Outline each blood parasite and name the species.
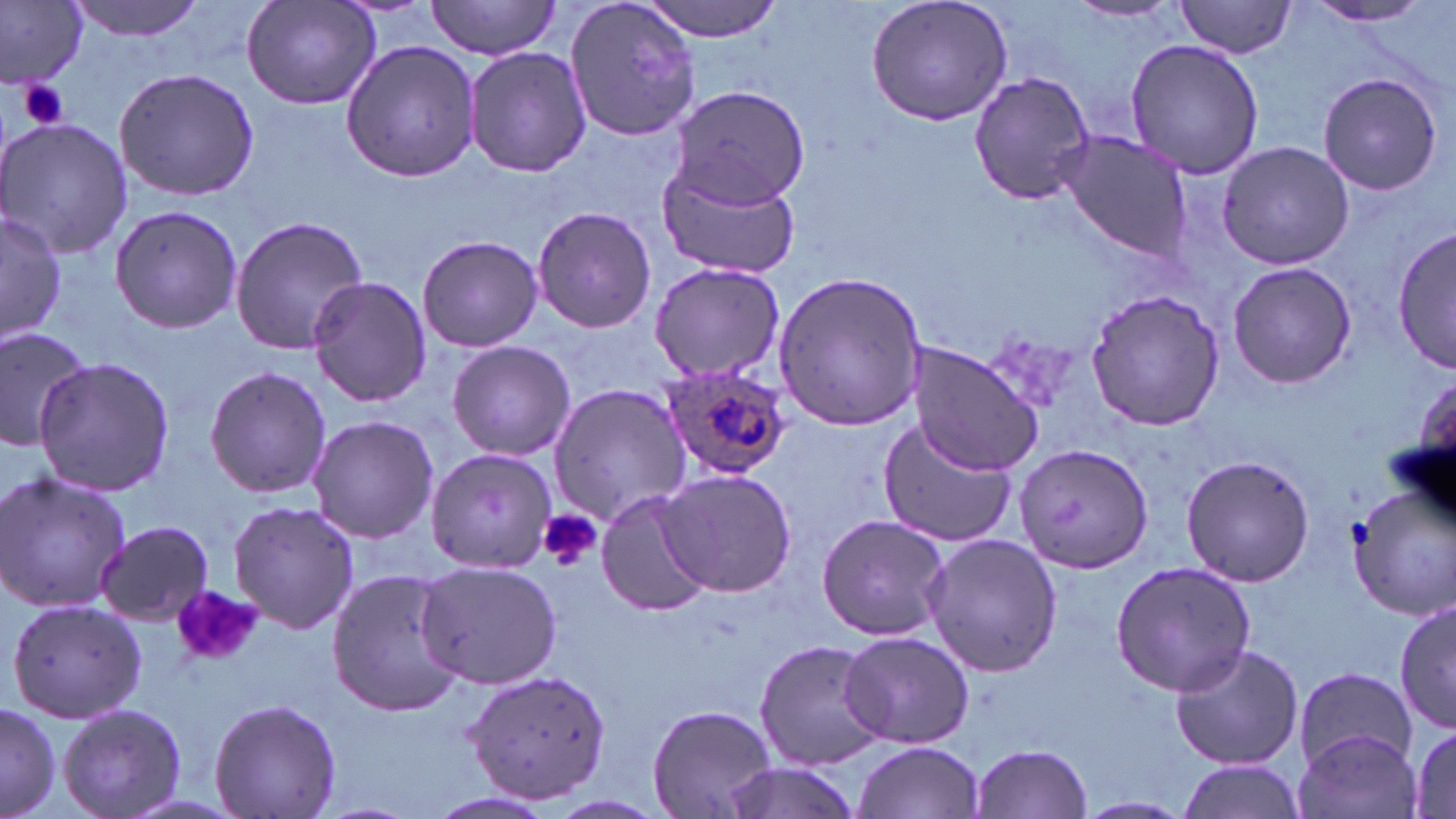

Approximate bounding boxes as named x1/y1/x2/y2 corners in pixels.
Plasmodium ovale-infected red blood cells: (x1=658, y1=363, x2=793, y2=482).
No Plasmodium falciparum, Plasmodium malariae, Plasmodium vivax, Babesia divergens, or Trypanosoma brucei observed.

{
  "slide_level_diagnosis": "Plasmodium ovale",
  "stain": "May-Grünwald-Giemsa",
  "modality": "optical microscopy",
  "platelet_locations": "approximate bounding boxes as named x1/y1/x2/y2 corners in pixels: (x1=16, y1=79, x2=70, y2=131), (x1=538, y1=509, x2=602, y2=571), (x1=175, y1=588, x2=265, y2=662)",
  "field_of_view": "one of a larger specimen",
  "preparation": "thin blood smear",
  "image_size": "1456×819 pixels",
  "magnification": "1000x",
  "uninfected_red_blood_cell_locations": "approximate bounding boxes as named x1/y1/x2/y2 corners in pixels: (x1=67, y1=0, x2=206, y2=41), (x1=425, y1=0, x2=560, y2=59), (x1=563, y1=0, x2=706, y2=143), (x1=640, y1=0, x2=783, y2=42), (x1=865, y1=0, x2=1014, y2=127), (x1=1175, y1=0, x2=1299, y2=59), (x1=0, y1=1, x2=90, y2=89), (x1=243, y1=1, x2=381, y2=112), (x1=1302, y1=1, x2=1438, y2=28), (x1=1067, y1=2, x2=1181, y2=25), (x1=339, y1=38, x2=482, y2=183), (x1=1123, y1=38, x2=1268, y2=180), (x1=464, y1=45, x2=593, y2=179), (x1=113, y1=66, x2=261, y2=201), (x1=967, y1=71, x2=1097, y2=204), (x1=1317, y1=71, x2=1443, y2=197), (x1=667, y1=84, x2=810, y2=207), (x1=1, y1=118, x2=133, y2=259), (x1=1055, y1=129, x2=1194, y2=261), (x1=1216, y1=139, x2=1355, y2=271), (x1=655, y1=158, x2=804, y2=279), (x1=107, y1=203, x2=242, y2=334), (x1=531, y1=205, x2=657, y2=335), (x1=2, y1=208, x2=66, y2=348), (x1=229, y1=216, x2=371, y2=356), (x1=1393, y1=226, x2=1455, y2=373), (x1=416, y1=235, x2=544, y2=352), (x1=648, y1=260, x2=786, y2=384), (x1=1226, y1=261, x2=1358, y2=389), (x1=770, y1=271, x2=927, y2=430), (x1=305, y1=276, x2=433, y2=408), (x1=1086, y1=287, x2=1224, y2=432), (x1=0, y1=321, x2=96, y2=450), (x1=446, y1=340, x2=576, y2=460), (x1=908, y1=342, x2=1042, y2=476), (x1=32, y1=356, x2=177, y2=497), (x1=202, y1=366, x2=332, y2=500), (x1=1409, y1=375, x2=1456, y2=496), (x1=547, y1=381, x2=693, y2=525), (x1=306, y1=415, x2=440, y2=541), (x1=875, y1=419, x2=1019, y2=552), (x1=1013, y1=445, x2=1152, y2=574), (x1=425, y1=447, x2=555, y2=573), (x1=1178, y1=453, x2=1316, y2=588), (x1=656, y1=467, x2=798, y2=598), (x1=0, y1=470, x2=133, y2=616), (x1=1349, y1=483, x2=1456, y2=625), (x1=594, y1=490, x2=713, y2=616), (x1=228, y1=501, x2=360, y2=634), (x1=816, y1=514, x2=951, y2=641), (x1=96, y1=520, x2=216, y2=627), (x1=923, y1=534, x2=1063, y2=677), (x1=1109, y1=559, x2=1256, y2=694), (x1=415, y1=560, x2=563, y2=686), (x1=325, y1=568, x2=463, y2=716), (x1=4, y1=595, x2=147, y2=723), (x1=1396, y1=601, x2=1454, y2=734), (x1=839, y1=630, x2=974, y2=750), (x1=752, y1=637, x2=886, y2=768), (x1=1169, y1=642, x2=1304, y2=769), (x1=1292, y1=666, x2=1417, y2=772), (x1=462, y1=667, x2=613, y2=805), (x1=209, y1=696, x2=341, y2=819), (x1=0, y1=700, x2=63, y2=819), (x1=59, y1=703, x2=187, y2=819), (x1=646, y1=704, x2=778, y2=819), (x1=1294, y1=729, x2=1422, y2=819), (x1=1407, y1=729, x2=1455, y2=815), (x1=854, y1=740, x2=985, y2=818), (x1=972, y1=743, x2=1093, y2=818), (x1=713, y1=759, x2=863, y2=819), (x1=1174, y1=759, x2=1307, y2=818), (x1=1074, y1=795, x2=1194, y2=818)"
}